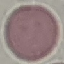
result: no malaria parasites detected
stain: Giemsa
image_type: cell patch, automatically extracted from a larger field of view and resized to 64 × 64 pixels
preparation: thin blood film
capture: smartphone through the microscope eyepiece